Locate and identify every blood parasite.
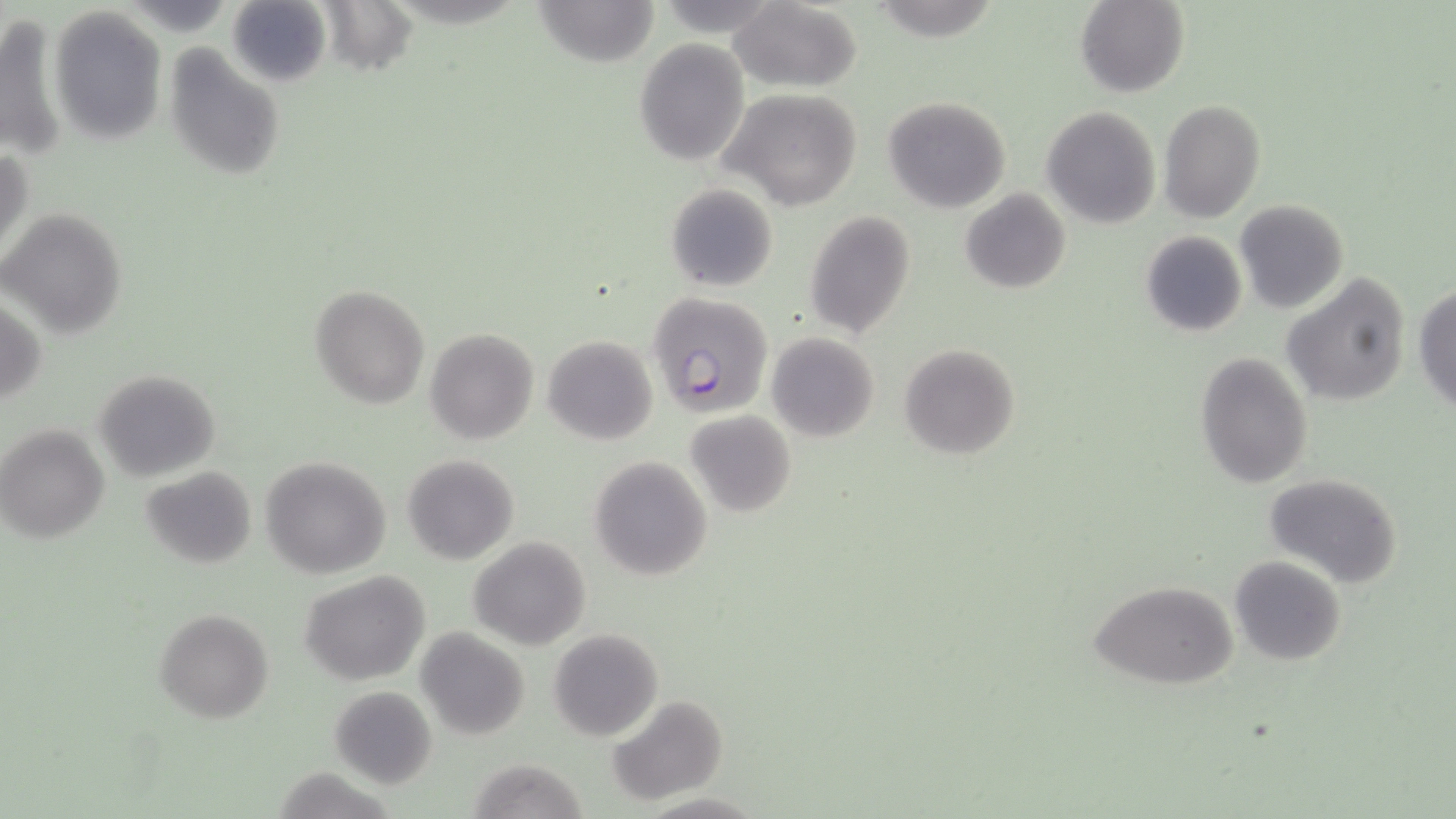

Approximate bounding boxes as (x1,y1)-(x2,y2) corner pairs in pixels.
Plasmodium falciparum-infected red blood cells: (648,292)-(773,418).
No Plasmodium ovale, Plasmodium malariae, Plasmodium vivax, Babesia divergens, or Trypanosoma brucei observed.

slide-level diagnosis = Plasmodium falciparum
preparation = thin blood smear
modality = light microscopy
image size = 1456×819 pixels
magnification = 1000x
field of view = one of a larger specimen
uninfected red blood cell locations = approximate bounding boxes as (x1,y1)-(x2,y2) corner pairs in pixels: (227,0)-(329,88), (532,0)-(659,67), (1076,0)-(1189,98), (318,1)-(418,74), (727,1)-(864,91), (50,5)-(167,144), (0,9)-(67,170), (634,39)-(751,165), (163,41)-(286,180), (722,90)-(863,209), (882,97)-(1011,213), (1159,100)-(1265,222), (1042,107)-(1161,229), (0,147)-(31,268), (664,183)-(778,292), (959,188)-(1071,295), (1234,200)-(1350,314), (1,208)-(127,338), (805,211)-(916,337), (1140,230)-(1247,338), (1282,274)-(1411,408), (1413,283)-(1456,413), (310,286)-(429,408), (1,294)-(46,412), (426,329)-(538,444), (766,332)-(879,442), (543,335)-(658,444), (898,343)-(1021,459), (1194,351)-(1313,488), (94,370)-(220,480), (684,410)-(797,517), (0,425)-(109,543), (402,454)-(519,565), (260,455)-(394,579), (589,455)-(711,582), (140,467)-(257,568), (1264,473)-(1402,587), (468,537)-(591,649), (1229,557)-(1346,665), (299,569)-(431,685), (1089,578)-(1240,691), (154,609)-(274,724), (549,628)-(664,742), (416,629)-(531,741), (328,686)-(437,787), (606,695)-(726,806), (469,757)-(588,819)
stain = May-Grünwald-Giemsa